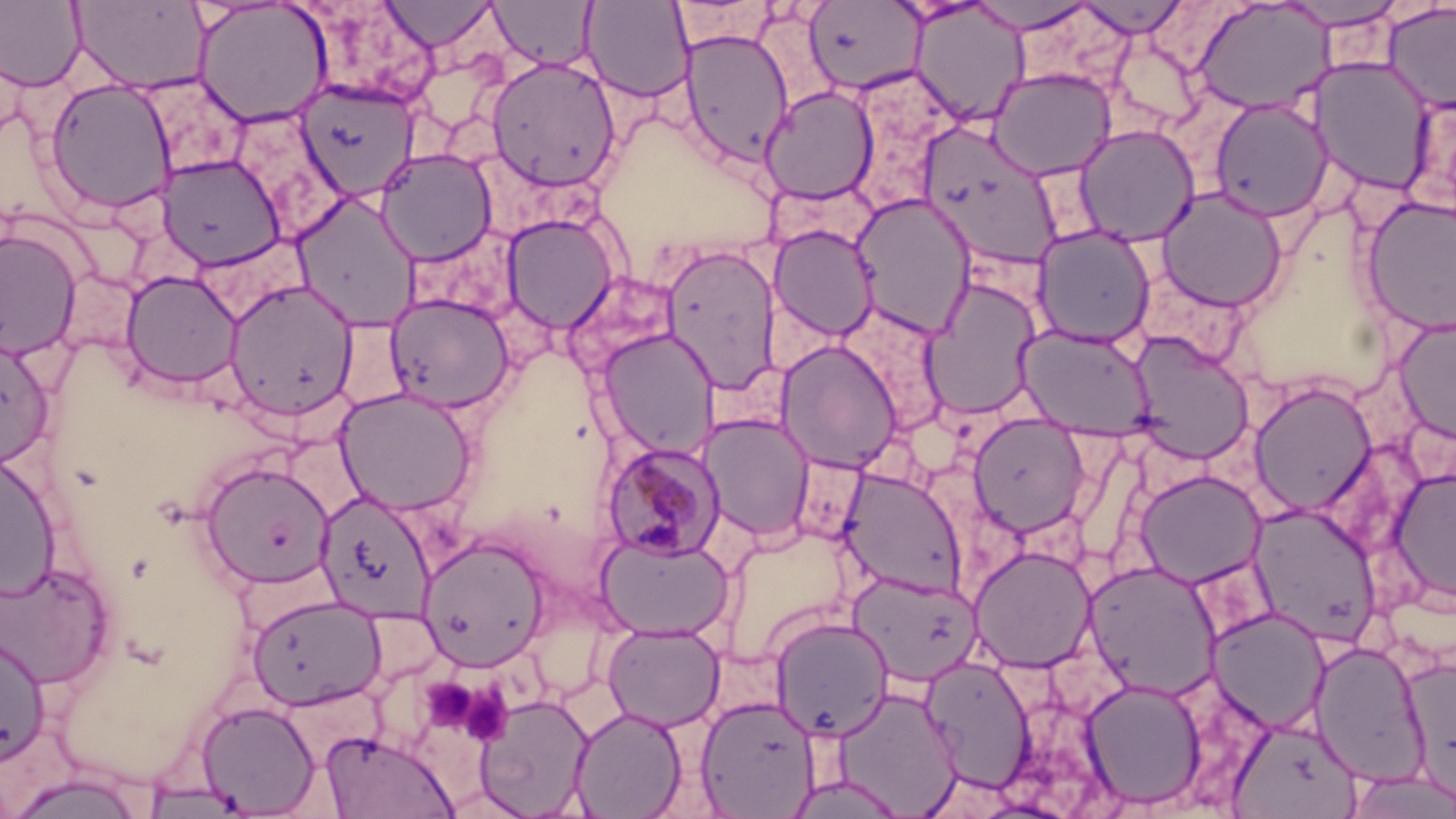
slide_level_diagnosis: Plasmodium malariae
magnification: 1000x
modality: optical microscopy
image_size: 1456×819 pixels
stain: May-Grünwald-Giemsa
platelet_locations: 'approximate bounding boxes as named x1/y1/x2/y2 corners in pixels: (x1=420, y1=677, x2=479, y2=729), (x1=458, y1=683, x2=513, y2=746)'
uninfected_red_blood_cell_locations: 'approximate bounding boxes as named x1/y1/x2/y2 corners in pixels: (x1=69, y1=0, x2=212, y2=95), (x1=490, y1=0, x2=598, y2=71), (x1=580, y1=0, x2=694, y2=103), (x1=1076, y1=0, x2=1191, y2=38), (x1=1192, y1=0, x2=1336, y2=116), (x1=0, y1=1, x2=86, y2=91), (x1=194, y1=1, x2=334, y2=127), (x1=378, y1=1, x2=500, y2=51), (x1=804, y1=1, x2=927, y2=96), (x1=967, y1=1, x2=1099, y2=34), (x1=1274, y1=1, x2=1410, y2=30), (x1=909, y1=2, x2=1031, y2=127), (x1=1383, y1=2, x2=1456, y2=114), (x1=679, y1=28, x2=794, y2=165), (x1=1109, y1=34, x2=1205, y2=134), (x1=486, y1=56, x2=621, y2=192), (x1=1308, y1=56, x2=1435, y2=196), (x1=987, y1=67, x2=1117, y2=180), (x1=43, y1=78, x2=178, y2=217), (x1=297, y1=80, x2=419, y2=202), (x1=759, y1=85, x2=880, y2=204), (x1=1209, y1=97, x2=1334, y2=221), (x1=224, y1=109, x2=351, y2=241), (x1=1070, y1=120, x2=1336, y2=235), (x1=917, y1=122, x2=1066, y2=270), (x1=1074, y1=124, x2=1200, y2=246), (x1=375, y1=148, x2=497, y2=264), (x1=156, y1=154, x2=287, y2=270), (x1=1156, y1=188, x2=1288, y2=312), (x1=291, y1=192, x2=421, y2=329), (x1=851, y1=194, x2=976, y2=339), (x1=1361, y1=195, x2=1456, y2=336), (x1=502, y1=214, x2=619, y2=333), (x1=769, y1=225, x2=879, y2=342), (x1=1032, y1=226, x2=1156, y2=348), (x1=0, y1=228, x2=82, y2=361), (x1=660, y1=244, x2=782, y2=394), (x1=120, y1=271, x2=243, y2=389), (x1=920, y1=276, x2=1043, y2=421), (x1=224, y1=280, x2=359, y2=422), (x1=385, y1=293, x2=515, y2=413), (x1=833, y1=302, x2=954, y2=436), (x1=1392, y1=315, x2=1456, y2=446), (x1=1018, y1=325, x2=1155, y2=439), (x1=597, y1=327, x2=719, y2=458), (x1=1128, y1=335, x2=1255, y2=465), (x1=0, y1=336, x2=55, y2=468), (x1=776, y1=340, x2=903, y2=473), (x1=1249, y1=381, x2=1377, y2=517), (x1=334, y1=387, x2=477, y2=516), (x1=699, y1=413, x2=816, y2=543), (x1=969, y1=414, x2=1091, y2=538), (x1=0, y1=454, x2=61, y2=600), (x1=199, y1=460, x2=336, y2=589), (x1=1387, y1=465, x2=1456, y2=607), (x1=839, y1=469, x2=967, y2=598), (x1=1134, y1=469, x2=1266, y2=587), (x1=314, y1=491, x2=437, y2=622), (x1=1248, y1=504, x2=1382, y2=647), (x1=597, y1=534, x2=733, y2=640), (x1=419, y1=536, x2=550, y2=670), (x1=970, y1=546, x2=1097, y2=672), (x1=0, y1=559, x2=115, y2=689), (x1=1084, y1=560, x2=1224, y2=701), (x1=849, y1=571, x2=983, y2=686), (x1=246, y1=593, x2=386, y2=709), (x1=1208, y1=606, x2=1331, y2=733), (x1=771, y1=615, x2=894, y2=740), (x1=602, y1=623, x2=725, y2=731), (x1=0, y1=634, x2=51, y2=766), (x1=1310, y1=640, x2=1430, y2=786), (x1=922, y1=655, x2=1036, y2=792), (x1=1402, y1=657, x2=1456, y2=805), (x1=1080, y1=677, x2=1207, y2=809), (x1=830, y1=684, x2=963, y2=817), (x1=475, y1=694, x2=594, y2=817), (x1=696, y1=694, x2=821, y2=817), (x1=196, y1=700, x2=320, y2=816), (x1=570, y1=705, x2=687, y2=819), (x1=1229, y1=716, x2=1363, y2=819), (x1=319, y1=729, x2=458, y2=818), (x1=1343, y1=769, x2=1456, y2=819), (x1=5, y1=771, x2=148, y2=819), (x1=784, y1=773, x2=910, y2=818), (x1=138, y1=781, x2=258, y2=818)'
preparation: thin blood film
field_of_view: one of a larger specimen
plasmodium_malariae_infected_red_blood_cell_locations: 'approximate bounding boxes as named x1/y1/x2/y2 corners in pixels: (x1=600, y1=441, x2=726, y2=561)'